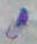

Summary:
  - Modality: micrograph
  - Identification: Toxoplasma gondii
  - Magnification: 1000x